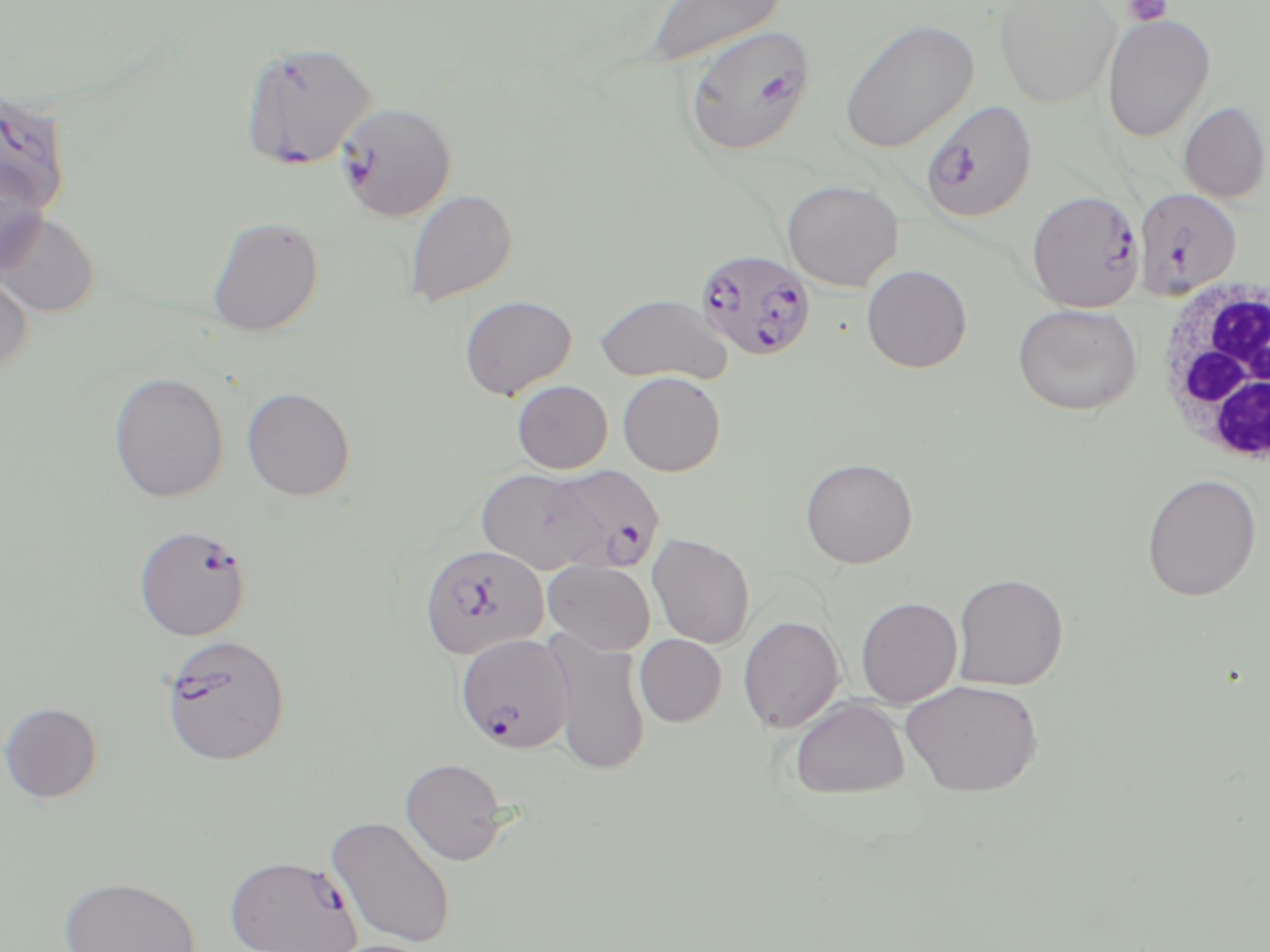
slide_level_diagnosis: Plasmodium falciparum
modality: light microscopy
field_of_view: single
preparation: thin blood smear
magnification: 1000x
plasmodium_falciparum_infected_red_blood_cell_locations: 'approximate bounding boxes as [x1, y1, x2, y2] in pixels: [681, 21, 814, 156], [238, 39, 378, 171], [0, 87, 72, 215], [919, 99, 1037, 224], [335, 102, 457, 221], [1133, 187, 1242, 299], [1026, 190, 1145, 312], [695, 248, 817, 361], [544, 464, 665, 573], [133, 523, 251, 641], [418, 543, 550, 659], [160, 633, 291, 766], [455, 633, 574, 754], [224, 853, 362, 952]'
stain: May-Grünwald-Giemsa
white_blood_cell_locations: 'approximate bounding boxes as [x1, y1, x2, y2] in pixels: [1150, 273, 1270, 469]'
image_size: 1270×952 pixels
uninfected_red_blood_cell_locations: 'approximate bounding boxes as [x1, y1, x2, y2] in pixels: [642, 0, 785, 68], [993, 0, 1121, 109], [1101, 13, 1216, 143], [838, 18, 979, 154], [1178, 101, 1270, 203], [0, 155, 49, 276], [781, 179, 904, 291], [404, 189, 518, 307], [0, 211, 100, 317], [206, 216, 324, 336], [861, 264, 972, 373], [0, 270, 34, 377], [593, 293, 732, 385], [459, 294, 577, 399], [1012, 302, 1144, 416], [108, 371, 229, 503], [617, 371, 726, 476], [512, 380, 613, 473], [241, 386, 356, 500], [800, 457, 918, 568], [477, 468, 604, 573], [1141, 473, 1263, 601], [647, 532, 755, 649], [543, 560, 656, 655], [953, 572, 1069, 690], [855, 596, 962, 707], [738, 616, 845, 733], [547, 631, 651, 777], [635, 634, 727, 726], [900, 679, 1043, 796], [790, 697, 910, 798], [0, 701, 104, 804], [400, 757, 508, 865], [325, 815, 457, 949], [58, 875, 203, 952], [318, 939, 437, 952]'
platelet_locations: 'approximate bounding boxes as [x1, y1, x2, y2] in pixels: [1123, 0, 1173, 26]'